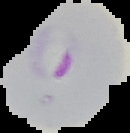 From a thin blood smear. Image is 130×133 pixels. Malaria status: parasitized. Segmented cell region on a black background.